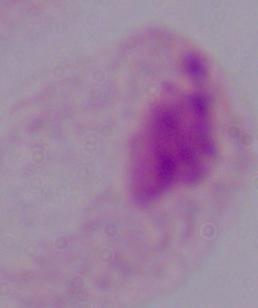
Summary:
  - Modality: photomicrograph
  - Identification: trichomonad
  - Magnification: 1000x